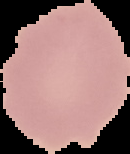
Summary:
  - Result: no malaria parasites detected
  - Image size: 130×154 pixels
  - Preparation: thin blood film
  - Image type: segmented cell region on a black background